Name the parasite shown.
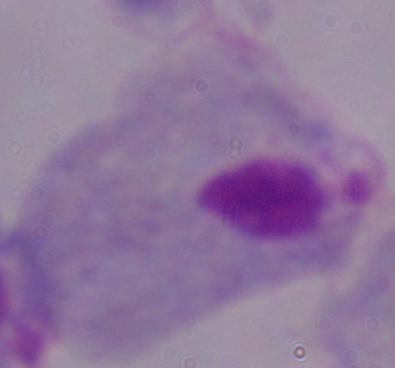
This is a trichomonad.

modality: photomicrograph
magnification: 1000x